Identify the cell.
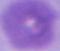
An erythrocyte.

magnification = 1000x
modality = micrograph